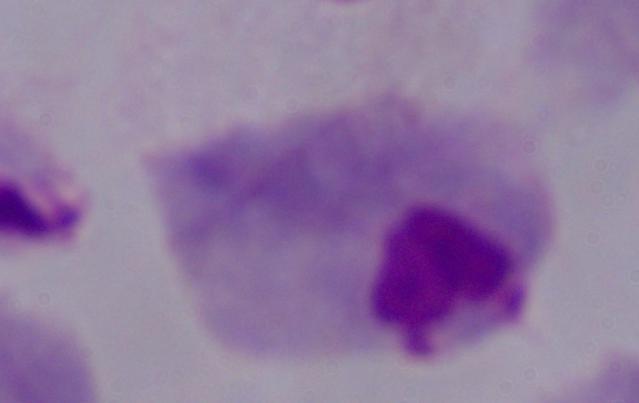
identification = trichomonad
magnification = 1000x
modality = photomicrograph